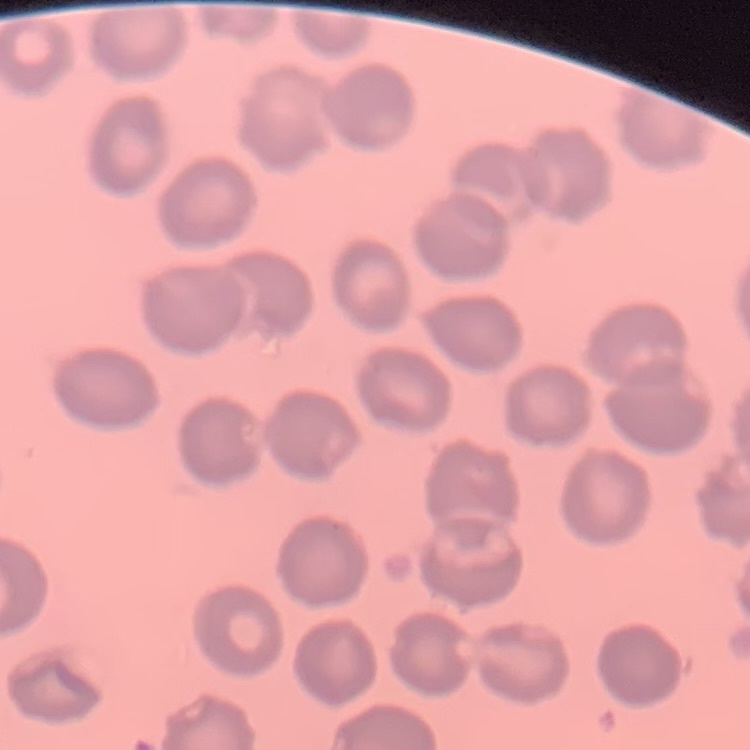 The erythrocytes exhibit no rouleaux formation. One tile cut from a larger photomicrograph. Thin peripheral smear. Field's or Giemsa stain.